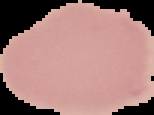
image size = 154×115 pixels
result = negative for Plasmodium parasites
preparation = thin blood film
image type = segmented cell region with the area outside set to black